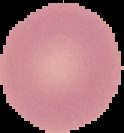
{
  "preparation": "thin blood smear",
  "image_type": "cell region segmented out of the field of view; surrounding area masked to black",
  "result": "no malaria parasites detected",
  "image_size": "124×133 pixels"
}